State which parasite is depicted.
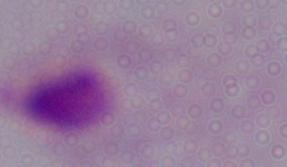

A trichomonad.

magnification: 1000x
modality: micrograph